Name the parasite shown.
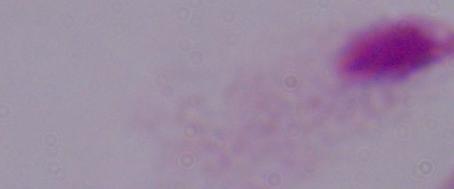

A trichomonad.

Summary:
  - Modality: micrograph
  - Magnification: 1000x